Comment on the morphology of the red blood cells.
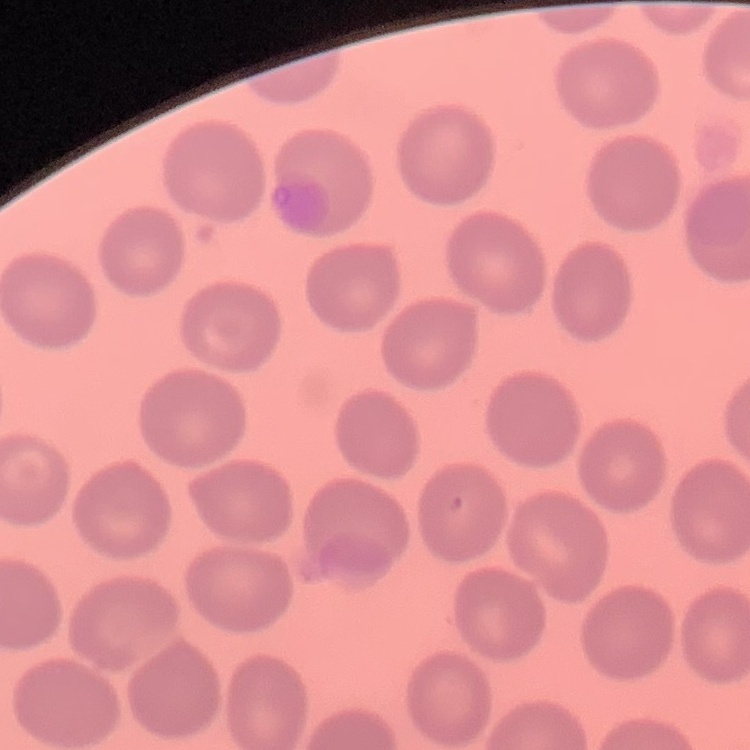

No rouleaux formation.

Summary:
  - Preparation: thin peripheral smear
  - Stain: Field's or Giemsa
  - Image type: square crop of a larger photomicrograph